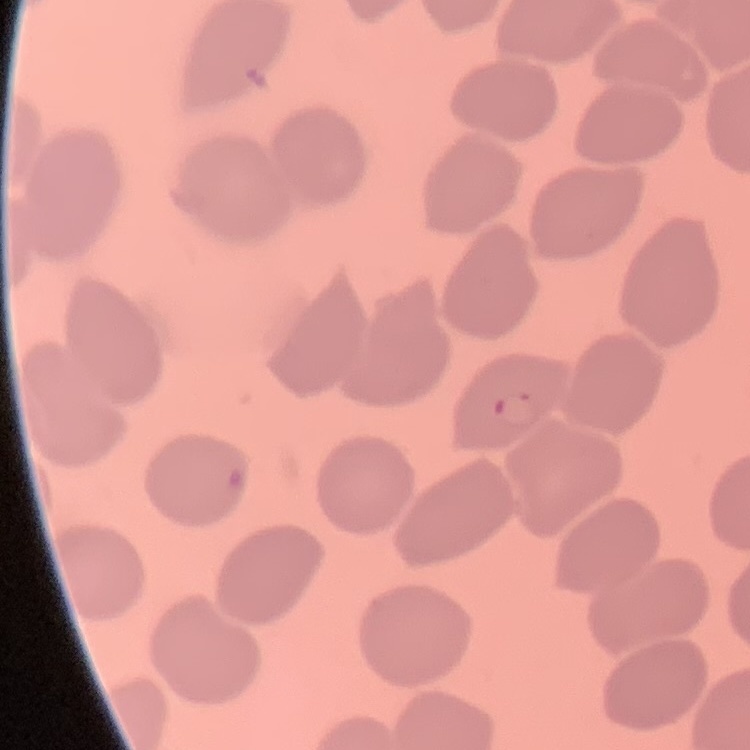
The erythrocytes exhibit no rouleaux formation. Square crop of a larger photomicrograph. Thin blood smear. Stained with either Field's or Giemsa.